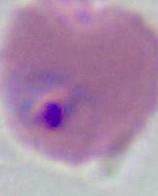 Photomicrograph. A Plasmodium parasite is shown. Captured at either 400x or 1000x magnification.